Locate every parasitized red blood cell.
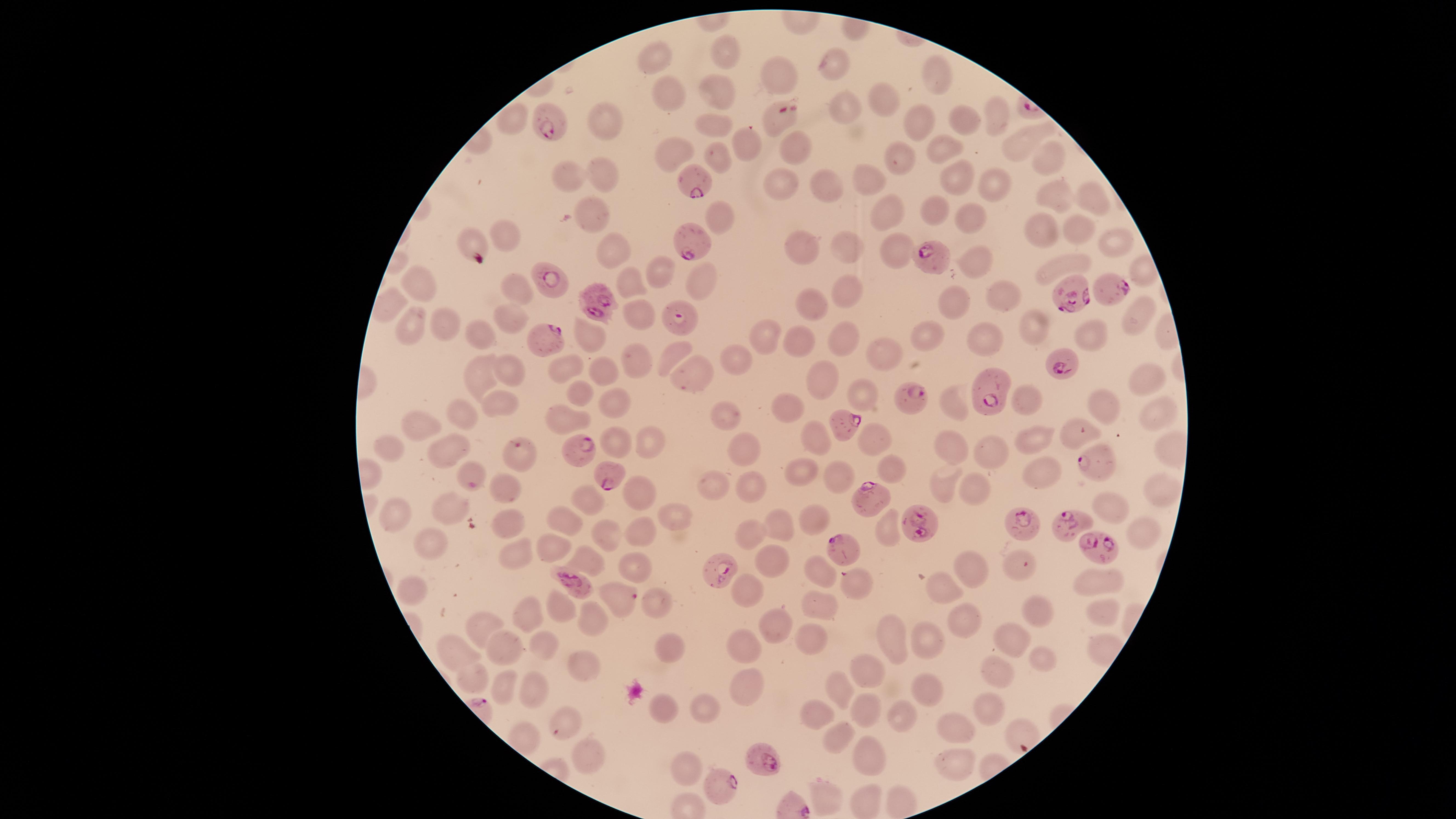
Approximate marker points as [x, y] in pixels.
Parasitized red blood cells: [551, 121], [698, 183], [690, 241], [932, 259], [547, 281], [1109, 287], [1069, 293], [600, 303], [679, 320], [540, 340], [1059, 361], [987, 396], [915, 401], [846, 425], [518, 449], [582, 451], [1092, 461], [607, 469], [872, 495], [923, 524], [1070, 524], [1026, 528], [1096, 544], [846, 549], [721, 569], [576, 580], [623, 596], [769, 761], [716, 783].

Approximate marker points as [x, y] in pixels. Uninfected red blood cells: [730, 48], [653, 52], [834, 67], [781, 72], [937, 76], [714, 85], [669, 92], [883, 97], [840, 103], [510, 114], [994, 114], [604, 120], [781, 120], [962, 120], [917, 121], [714, 122], [1017, 140], [743, 143], [793, 147], [943, 147], [666, 150], [1048, 155], [719, 157], [903, 160], [571, 175], [608, 175], [870, 179], [959, 179], [782, 180], [992, 185], [829, 186], [1088, 194], [1049, 198], [592, 205], [931, 210], [895, 213], [724, 218], [974, 219], [1078, 228], [1036, 229], [505, 231], [1114, 238], [846, 244], [896, 247], [609, 249], [802, 249], [973, 259], [1065, 265], [662, 273], [701, 279], [627, 281], [421, 283], [516, 284], [846, 285], [1001, 294], [813, 303], [958, 304], [638, 312], [1142, 314], [513, 315], [445, 323], [415, 324], [1033, 330], [846, 333], [1092, 334], [589, 336], [762, 336], [984, 336], [799, 337], [930, 337], [485, 340], [884, 352], [671, 354], [734, 358], [570, 364], [632, 364], [511, 368], [606, 370], [486, 374], [693, 376], [1142, 381], [818, 383], [584, 392], [860, 393], [1024, 398], [615, 399], [497, 404], [950, 404], [720, 405], [782, 408], [1103, 408], [1160, 408], [465, 413], [421, 429], [1031, 434], [1073, 436], [815, 437], [873, 437], [617, 439], [653, 440], [747, 446], [954, 447], [390, 448], [987, 449], [442, 453], [891, 467], [804, 469], [465, 470], [839, 474], [942, 476], [1042, 476], [711, 483], [504, 485], [748, 486], [1160, 486], [972, 488], [637, 490], [584, 494], [444, 502], [1109, 505], [394, 509], [671, 513], [813, 517], [560, 519], [501, 523], [775, 523], [644, 527], [754, 532], [601, 535], [1136, 539], [550, 541], [428, 551], [514, 554], [766, 556], [583, 557], [1016, 559], [633, 565], [967, 566], [817, 567], [1094, 581], [859, 585], [944, 589], [747, 590], [407, 592], [558, 601], [656, 602], [822, 604], [1033, 606], [1098, 609], [531, 612], [593, 614], [962, 619], [772, 624], [486, 626], [895, 633], [1012, 634], [923, 640], [543, 641], [808, 642], [502, 647], [744, 647], [453, 648], [674, 648], [1037, 654], [580, 663], [864, 669], [995, 673], [475, 678], [509, 685], [532, 686], [739, 686], [837, 690], [926, 691], [657, 709], [867, 710], [991, 710], [705, 713], [560, 714], [813, 716], [901, 716], [952, 725], [1020, 727], [836, 737], [867, 757], [591, 761], [952, 764], [684, 773], [828, 796], [869, 799]. Photographed with a smartphone camera through the microscope eyepiece. Image is 1456×819 pixels. Species: Plasmodium falciparum. Circular visible region. Thin blood film. Giemsa stain. Single field of view.